Comment on the morphology of the erythrocytes.
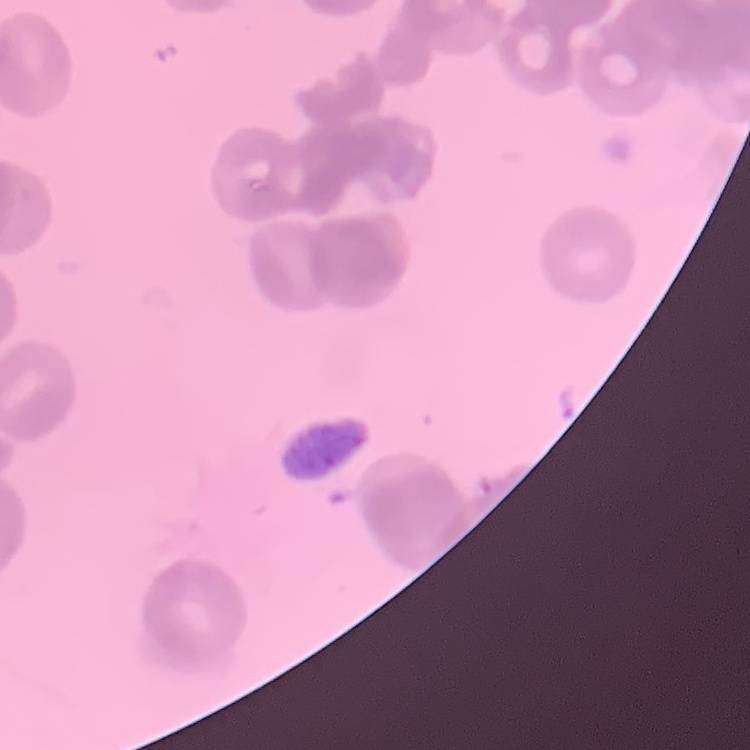

They show rouleaux formation.

Summary:
  - Stain: Field's or Giemsa
  - Preparation: thin blood smear
  - Image type: square crop of a larger photomicrograph